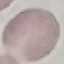

Malaria status: uninfected. Giemsa stain. Photographed with a smartphone camera at the microscope eyepiece. Automatically extracted cell patch, resized to 64 × 64 pixels. Thin blood smear.